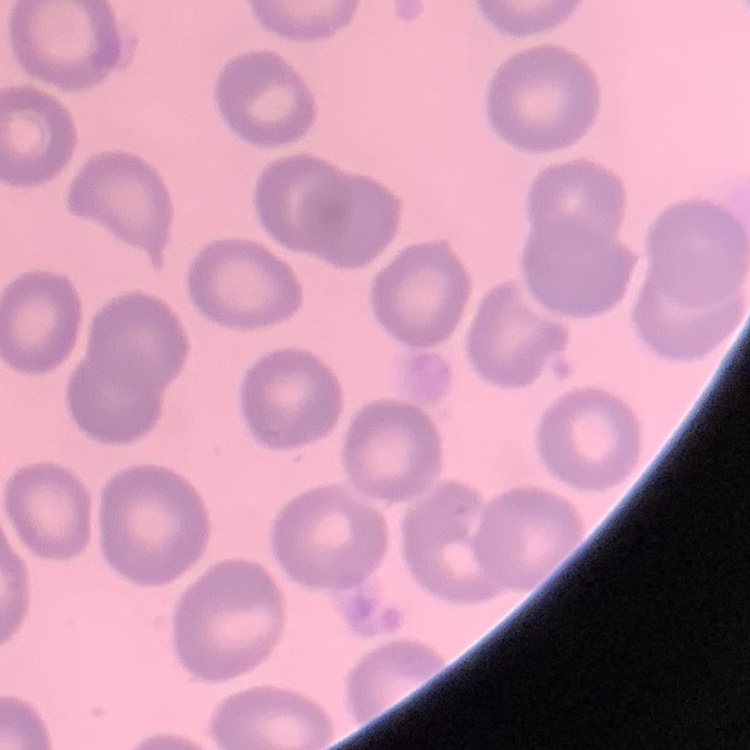 The erythrocytes show no rouleaux formation. One tile cut from a larger photomicrograph. Thin blood film. Field's or Giemsa stain.